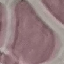
malaria status = uninfected
capture = smartphone through the microscope eyepiece
image type = cell patch, automatically extracted from a larger field of view and resized to 64 × 64 pixels
preparation = thin smear
stain = Giemsa